Locate every blood parasite and identify its species.
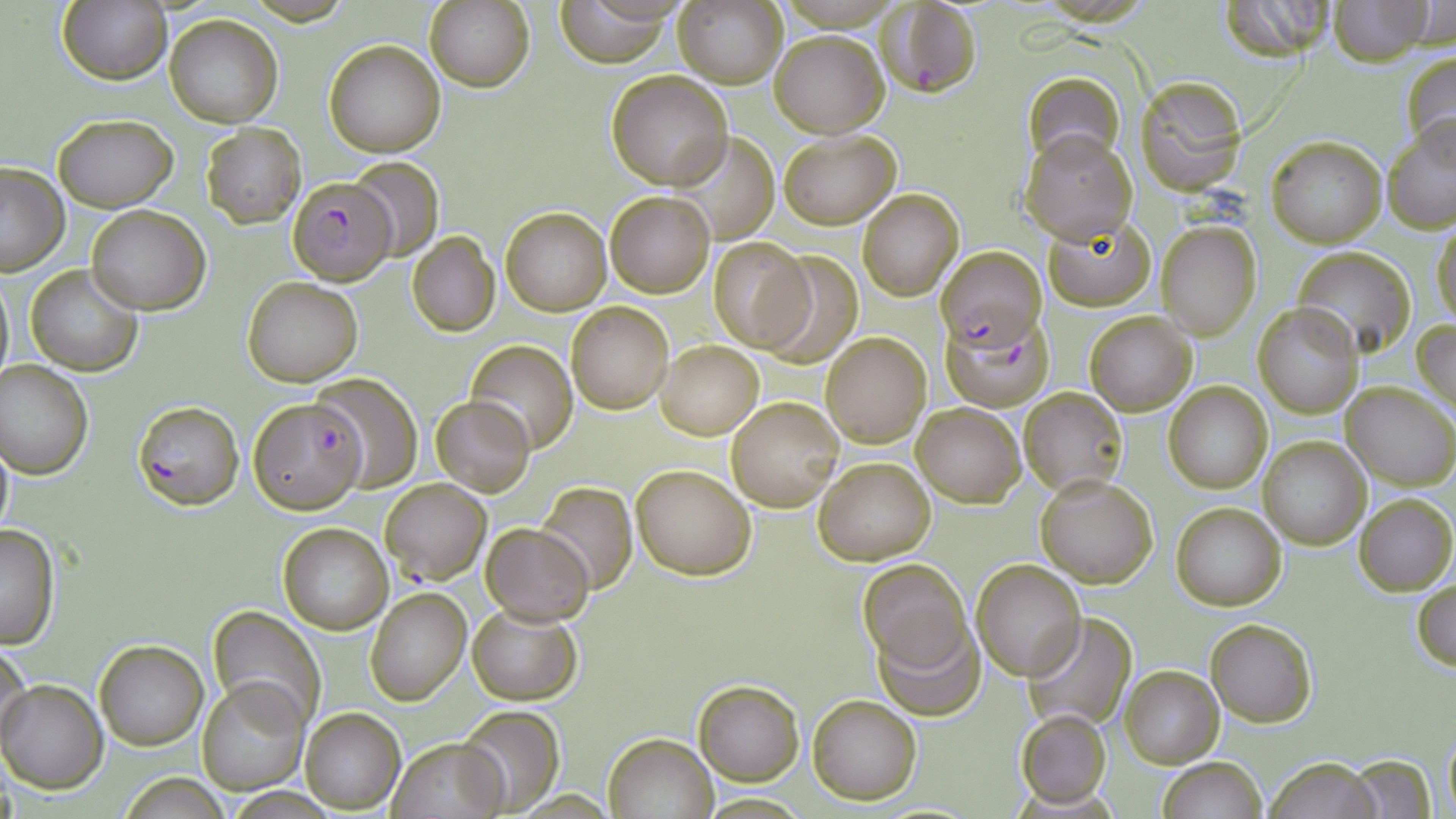
Approximate bounding boxes as (x1, y1, x2, y2) in pixels.
Plasmodium falciparum-infected red blood cells: (878, 1, 982, 96), (287, 176, 396, 285), (941, 244, 1046, 350), (944, 313, 1053, 412), (248, 396, 366, 515), (133, 400, 244, 510), (380, 478, 491, 586).
No Plasmodium ovale, Plasmodium malariae, Plasmodium vivax, Babesia divergens, or Trypanosoma brucei observed.

Uninfected red blood cell locations: (59, 0, 172, 85), (675, 0, 788, 88), (1221, 0, 1342, 58), (1326, 0, 1434, 67), (426, 1, 536, 92), (554, 2, 677, 64), (1417, 3, 1454, 47), (164, 14, 283, 127), (770, 31, 888, 137), (323, 38, 447, 158), (1399, 49, 1456, 161), (605, 70, 731, 188), (1024, 73, 1125, 167), (1133, 76, 1246, 194), (52, 113, 177, 211), (1384, 120, 1456, 234), (201, 124, 305, 228), (1020, 129, 1139, 243), (779, 130, 900, 228), (667, 131, 782, 244), (1266, 135, 1386, 247), (348, 158, 445, 260), (0, 162, 71, 275), (857, 188, 964, 300), (605, 191, 714, 297), (87, 204, 210, 315), (500, 206, 612, 316), (1044, 219, 1156, 310), (1156, 220, 1260, 339), (1431, 221, 1456, 331), (408, 232, 499, 336), (707, 238, 813, 352), (1293, 247, 1417, 357), (756, 250, 864, 368), (25, 264, 142, 376), (0, 267, 13, 392), (242, 277, 362, 386), (1252, 302, 1364, 418), (567, 303, 673, 413), (1083, 310, 1196, 415), (1413, 319, 1456, 417), (822, 332, 931, 448), (466, 340, 578, 452), (657, 341, 763, 439), (0, 360, 94, 478), (311, 374, 422, 492), (1164, 382, 1272, 494), (1342, 382, 1455, 487), (1019, 388, 1128, 496), (429, 395, 536, 497), (727, 396, 845, 511), (912, 401, 1026, 507), (0, 430, 14, 546), (1259, 436, 1370, 550), (815, 457, 934, 565), (631, 463, 756, 580), (1035, 475, 1159, 587), (538, 483, 636, 595), (1355, 493, 1455, 596), (1172, 502, 1287, 610), (482, 522, 594, 623), (0, 523, 59, 650), (278, 524, 392, 634), (858, 559, 972, 674), (971, 559, 1084, 679), (1412, 577, 1456, 673), (365, 588, 472, 706), (467, 605, 582, 704), (207, 606, 326, 729), (1022, 613, 1140, 731), (872, 616, 985, 719), (1206, 617, 1317, 729), (94, 640, 208, 751), (0, 642, 32, 756), (1119, 664, 1223, 768), (196, 677, 309, 794), (1, 679, 107, 793), (694, 679, 805, 785), (807, 693, 922, 805), (456, 705, 565, 815), (300, 708, 405, 813), (1014, 709, 1112, 807), (1442, 730, 1455, 816), (603, 732, 719, 819), (387, 736, 508, 818), (1348, 754, 1436, 817), (1157, 757, 1267, 818), (1263, 757, 1384, 818), (117, 774, 232, 818). Slide-level diagnosis: Plasmodium falciparum. 1000x magnification. May-Grünwald-Giemsa-stained preparation. Image is 1456×819 pixels. Single field of view. Thin blood film. Light microscopy.